Assess this cell for malaria.
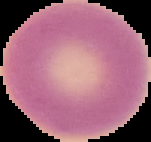
Uninfected.

image_type: segmented cell region on a black background
preparation: thin blood smear
image_size: 151×142 pixels